State which parasite is depicted.
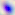

Toxoplasma gondii.

Micrograph. Captured at 400x magnification.